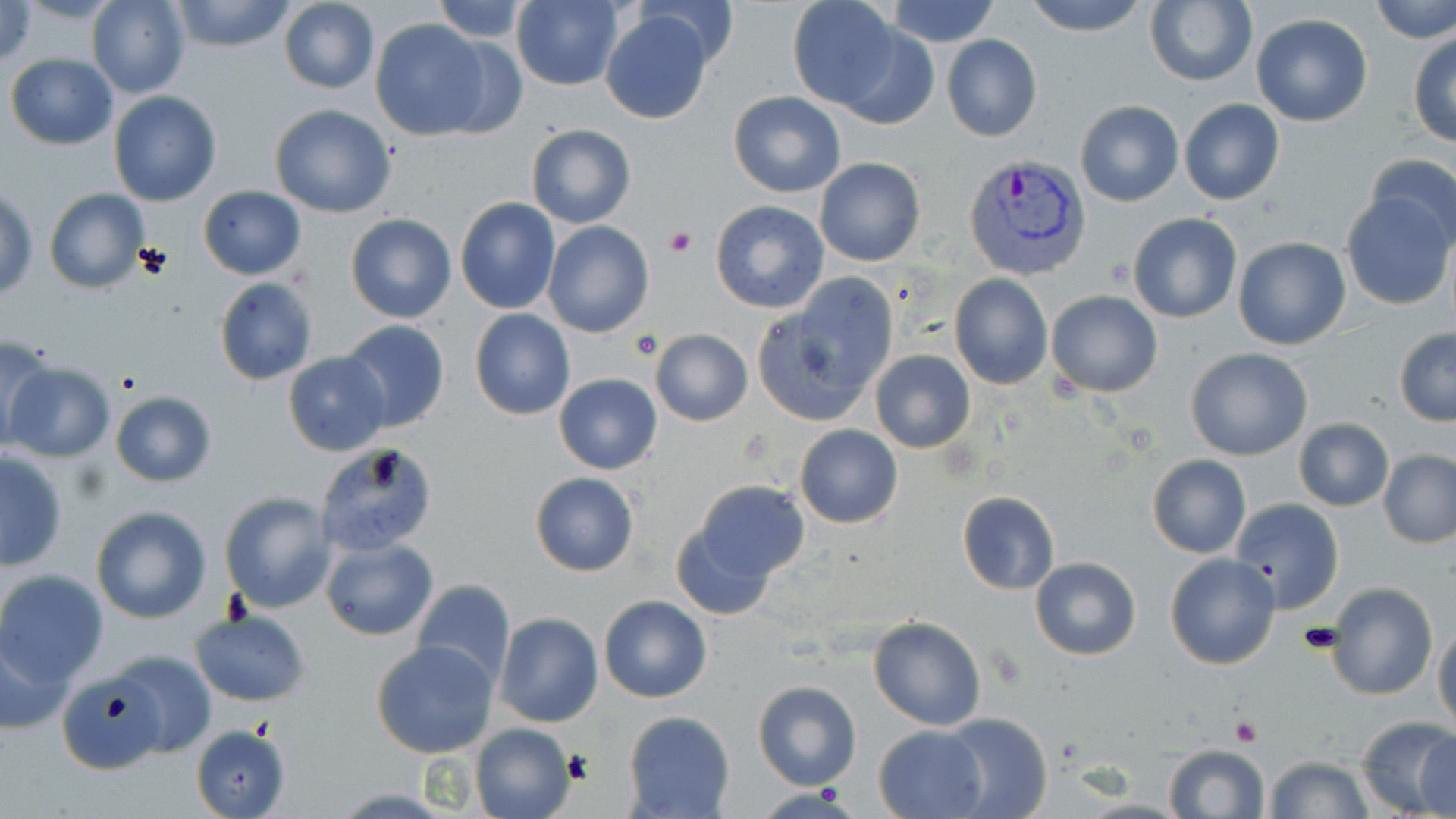

Approximate bounding boxes as (x1, y1, x2, y2) in pixels. Uninfected red blood cell locations: (170, 0, 299, 52), (431, 0, 531, 42), (884, 0, 1000, 47), (1021, 0, 1152, 35), (1369, 0, 1456, 45), (0, 1, 37, 66), (86, 1, 191, 99), (279, 1, 378, 95), (510, 1, 623, 89), (789, 1, 905, 113), (1144, 1, 1259, 89), (637, 2, 741, 69), (601, 11, 713, 124), (1251, 14, 1373, 127), (371, 18, 491, 140), (827, 20, 940, 131), (1408, 33, 1456, 147), (942, 35, 1042, 142), (431, 39, 526, 137), (5, 53, 118, 151), (728, 90, 846, 198), (108, 92, 224, 207), (1178, 99, 1286, 206), (1074, 100, 1184, 207), (268, 104, 398, 218), (526, 124, 635, 228), (1364, 151, 1456, 254), (814, 158, 925, 267), (197, 186, 306, 280), (0, 188, 38, 299), (44, 188, 150, 295), (1340, 191, 1454, 311), (454, 197, 562, 315), (710, 199, 829, 313), (346, 212, 457, 324), (1128, 212, 1242, 323), (543, 221, 654, 338), (1232, 238, 1352, 351), (753, 274, 900, 426), (949, 274, 1053, 390), (214, 278, 317, 386), (1046, 289, 1161, 397), (470, 309, 575, 420), (338, 321, 451, 434), (1393, 327, 1456, 426), (651, 329, 753, 425), (0, 333, 58, 451), (1184, 346, 1313, 460), (870, 349, 976, 453), (283, 351, 391, 455), (5, 363, 115, 463), (553, 373, 661, 475), (109, 391, 217, 487), (1294, 418, 1393, 510), (794, 425, 903, 528), (314, 443, 439, 557), (1378, 449, 1456, 548), (0, 452, 68, 570), (1146, 454, 1252, 559), (530, 472, 638, 577), (691, 480, 809, 580), (955, 490, 1059, 595), (219, 491, 337, 613), (1230, 497, 1345, 613), (90, 506, 212, 624), (670, 516, 781, 621), (321, 538, 438, 640), (1165, 553, 1281, 669), (1029, 556, 1142, 660), (0, 569, 108, 687), (410, 578, 516, 687), (1327, 580, 1437, 701), (599, 596, 711, 703), (190, 610, 310, 707), (495, 612, 603, 727), (868, 616, 987, 730), (1432, 627, 1456, 730), (0, 629, 75, 737), (370, 639, 498, 758), (112, 650, 217, 759), (57, 671, 167, 774), (752, 680, 862, 791), (625, 711, 735, 819), (939, 713, 1053, 819), (1355, 716, 1456, 819), (470, 723, 576, 819), (189, 724, 290, 818), (874, 725, 987, 818), (1415, 734, 1454, 818), (1162, 744, 1271, 819), (1264, 756, 1375, 817). Plasmodium vivax-infected red blood cell locations: (961, 153, 1093, 282). Platelet locations: (663, 225, 695, 257), (631, 333, 661, 359), (1231, 717, 1262, 746). Slide-level diagnosis: Plasmodium vivax. Image is 1456×819 pixels. Thin blood smear. May-Grünwald-Giemsa-stained preparation. Optical microscopy. 1000x magnification. Single field of view.